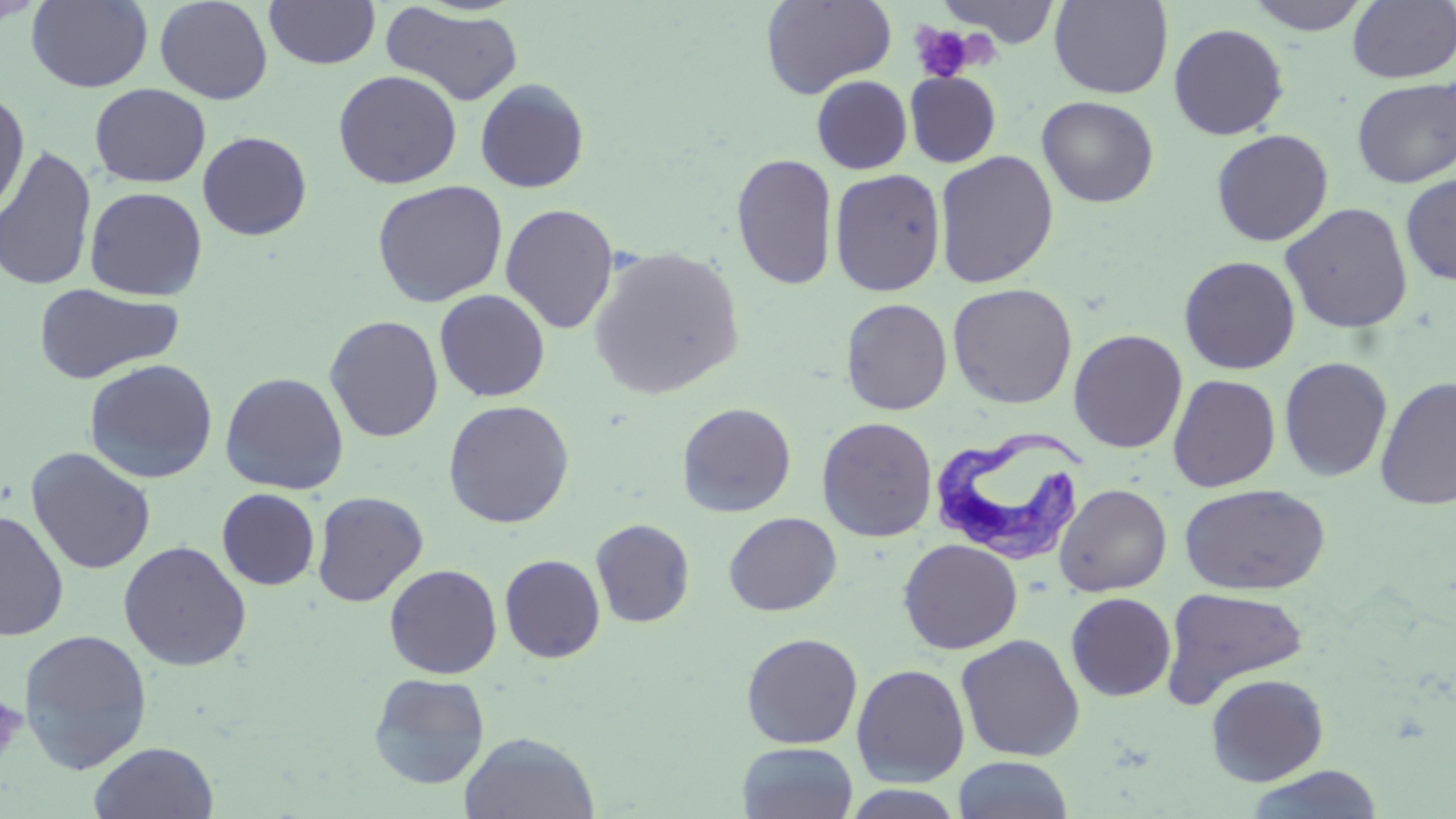
slide-level diagnosis = Trypanosoma brucei
image size = 1456×819 pixels
magnification = 1000x
field of view = single
modality = optical microscopy
uninfected red blood cell locations = approximate bounding boxes as [x1, y1, x2, y2] in pixels: [1, 0, 47, 26], [26, 0, 153, 93], [155, 0, 273, 104], [263, 0, 380, 70], [760, 0, 896, 99], [938, 0, 1062, 48], [1244, 0, 1374, 35], [1049, 1, 1174, 99], [1348, 1, 1456, 84], [381, 4, 525, 106], [1168, 23, 1289, 140], [333, 70, 462, 189], [904, 70, 1002, 168], [811, 75, 912, 174], [475, 78, 590, 193], [1352, 78, 1455, 188], [90, 83, 211, 188], [0, 90, 30, 218], [1036, 95, 1159, 207], [1211, 128, 1334, 246], [197, 131, 312, 240], [0, 145, 98, 292], [934, 150, 1059, 288], [731, 153, 838, 291], [830, 168, 946, 296], [1400, 172, 1456, 286], [372, 180, 508, 307], [84, 186, 208, 301], [1280, 202, 1414, 333], [500, 204, 619, 334], [588, 246, 745, 399], [1178, 255, 1301, 375], [947, 282, 1078, 409], [33, 283, 183, 384], [434, 289, 551, 402], [840, 298, 952, 415], [324, 315, 444, 442], [1068, 328, 1188, 453], [1278, 356, 1393, 483], [83, 359, 218, 484], [220, 371, 350, 495], [1167, 374, 1281, 492], [1375, 376, 1456, 511], [443, 399, 575, 528], [677, 402, 797, 517], [817, 416, 938, 541], [25, 447, 157, 575], [1054, 483, 1172, 597], [1178, 483, 1330, 596], [216, 488, 320, 591], [311, 491, 428, 606], [0, 510, 69, 641], [723, 511, 842, 616], [591, 519, 695, 628], [898, 539, 1023, 654], [117, 540, 252, 670], [499, 554, 605, 663], [384, 564, 502, 679], [1160, 586, 1310, 707], [1065, 592, 1176, 701], [17, 628, 153, 775], [741, 632, 863, 749], [955, 634, 1086, 762], [851, 663, 970, 787], [368, 672, 490, 790], [1206, 673, 1329, 786], [459, 731, 600, 819], [88, 741, 219, 819], [737, 742, 859, 819], [952, 756, 1074, 819], [1242, 765, 1386, 819], [838, 784, 970, 818]
stain = May-Grünwald-Giemsa
platelet locations = approximate bounding boxes as [x1, y1, x2, y2] in pixels: [908, 22, 982, 82], [0, 691, 26, 768]
Trypanosoma brucei locations = approximate bounding boxes as [x1, y1, x2, y2] in pixels: [928, 430, 1090, 569]
preparation = thin blood smear